Assess this cell for malaria.
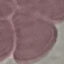
It is uninfected.

Summary:
  - Image type: cell patch, automatically extracted from a larger field of view and resized to 64 × 64 pixels
  - Preparation: thin blood film
  - Stain: Giemsa
  - Capture: smartphone camera at the microscope eyepiece